Comment on the morphology of the red blood cells.
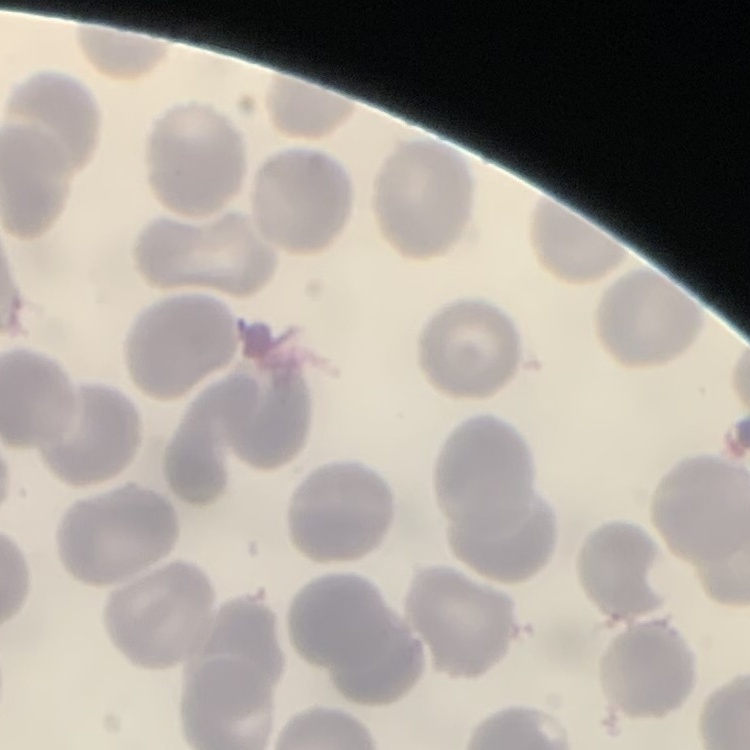

They show no rouleaux formation.

image type = one tile cut from a larger photomicrograph
stain = Field's or Giemsa
preparation = thin peripheral smear